Look for parasitized red blood cells.
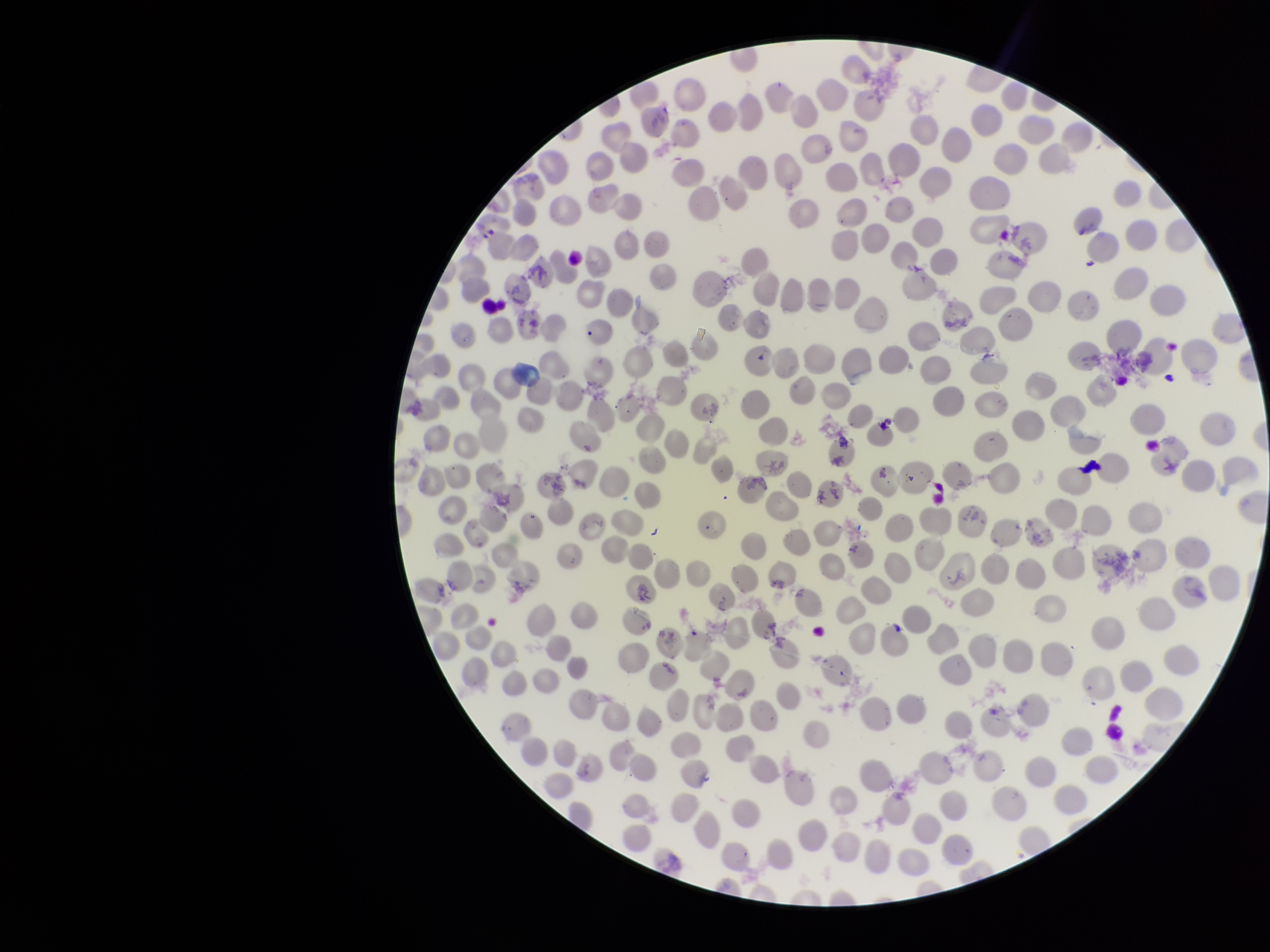

None identified.

Patient malaria status: positive. Parasitized red blood cell count: 0. Image is 1270×952 pixels. Giemsa stain. Red blood cell count: 283. Photographed through the microscope eyepiece with a smartphone camera. Species reported for this patient: Plasmodium vivax. Single field of view. Preparation: thin blood smear.